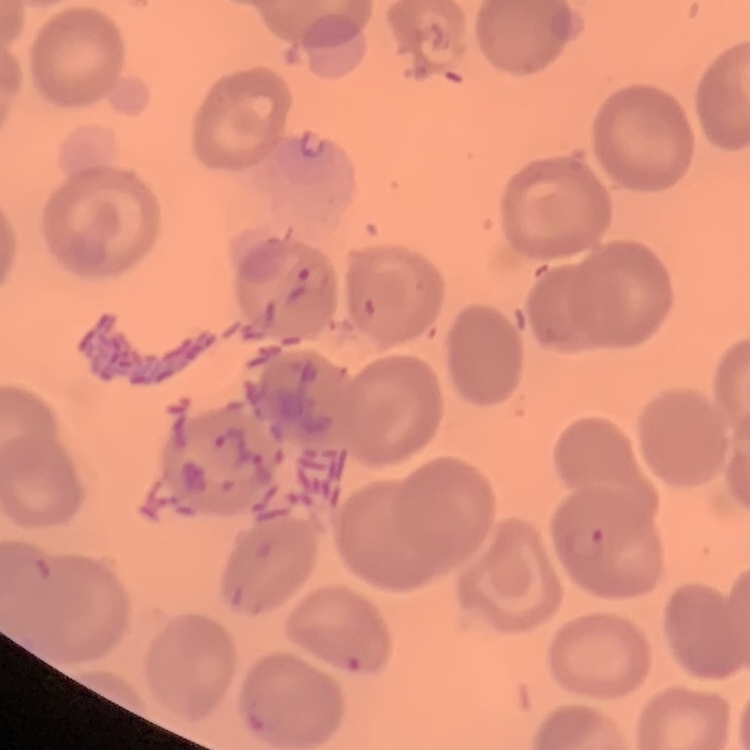
red blood cell morphology = no rouleaux formation
preparation = thin blood film
stain = Field's or Giemsa
image type = square crop of a larger photomicrograph